Describe the morphology of the red blood cells.
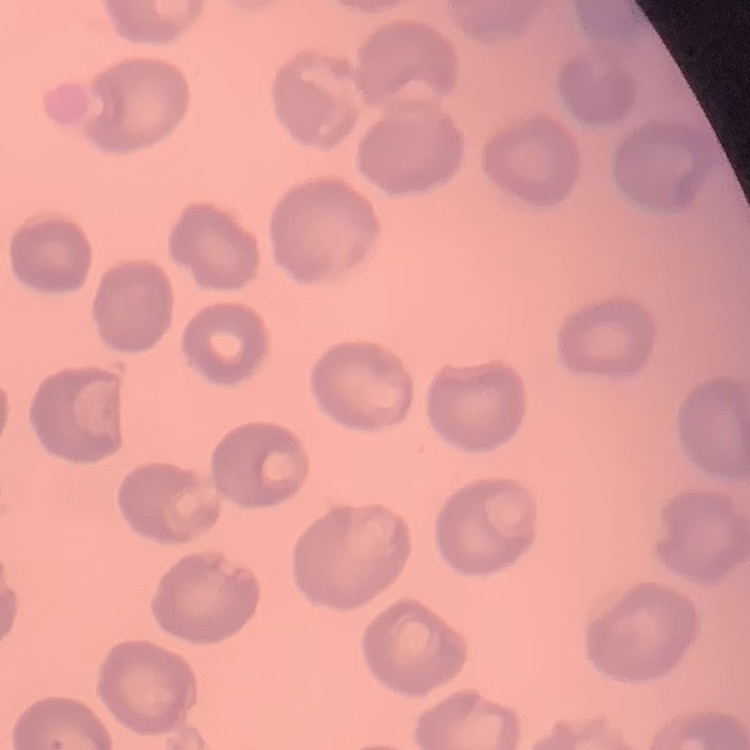
They show no rouleaux formation.

preparation = thin blood smear
image type = square crop of a larger photomicrograph
stain = Field's or Giemsa